Comment on the morphology of the red blood cells.
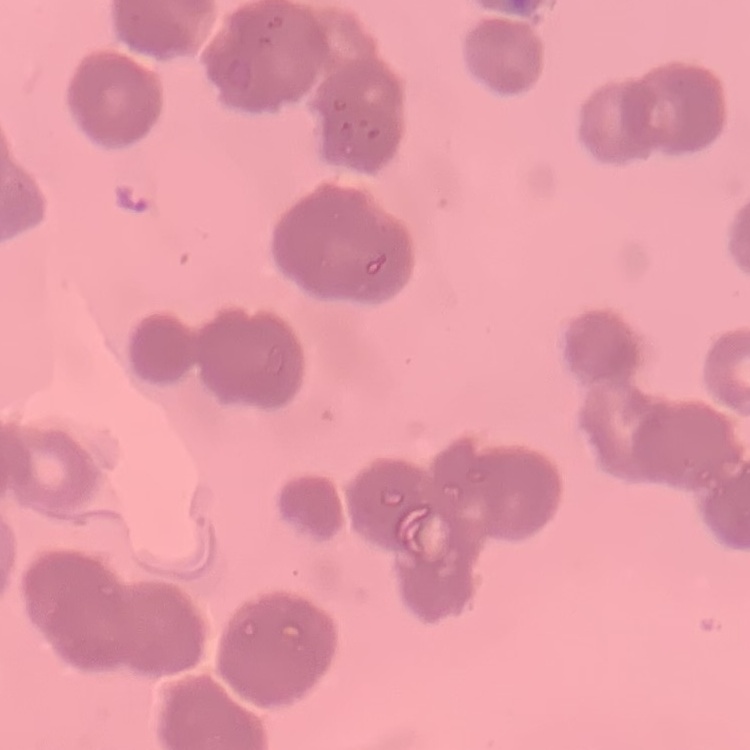

Rouleaux formation.

stain: Field's or Giemsa
image_type: one tile cut from a larger photomicrograph
preparation: thin peripheral smear